Identify the cell.
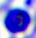
This is a leukocyte.

Summary:
  - Modality: micrograph
  - Magnification: 400x